Locate every leukocyte (white blood cell).
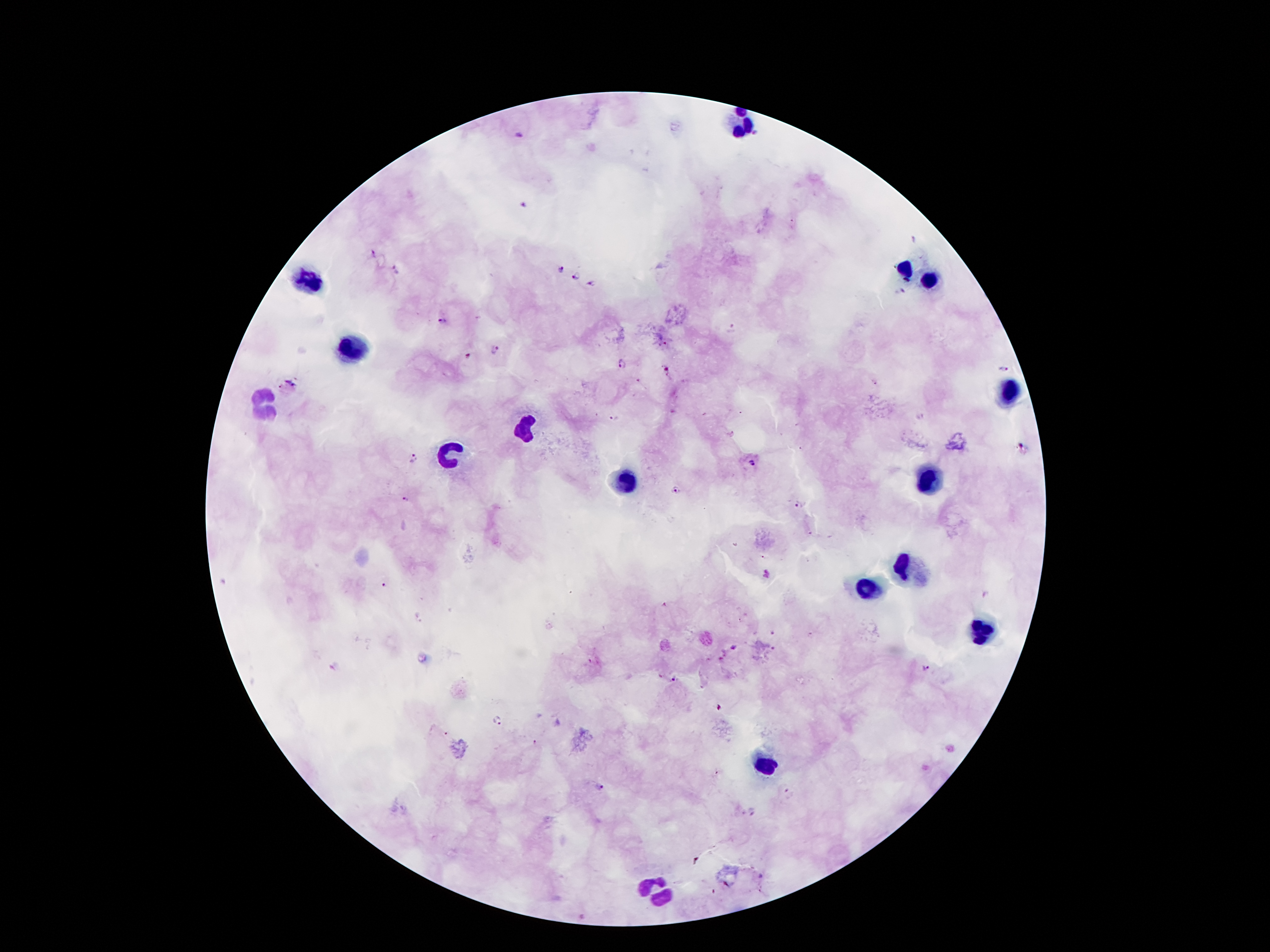

Approximate centers as {x, y} in pixels.
Leukocytes: {745, 123}, {907, 272}, {311, 281}, {929, 281}, {352, 353}, {1010, 390}, {268, 400}, {524, 428}, {444, 451}, {934, 480}, {625, 483}, {899, 569}, {865, 587}, {981, 632}, {766, 763}, {655, 890}.

{
  "magnification": "100x",
  "image_size": "1270×952 pixels",
  "preparation": "thick blood smear",
  "stain": "Giemsa",
  "capture": "smartphone through the microscope eyepiece",
  "patient_malaria_status": "positive for Plasmodium falciparum",
  "malaria_parasite_locations": "approximate centers as {x, y} in pixels: {756, 134}, {519, 135}, {371, 253}, {561, 268}, {396, 270}, {576, 276}, {592, 285}, {900, 293}, {441, 322}, {731, 328}, {496, 349}, {469, 356}, {623, 363}, {1001, 368}, {872, 383}, {614, 419}, {412, 459}, {753, 463}, {674, 490}, {408, 500}, {799, 505}, {767, 574}, {383, 585}, {772, 635}, {733, 649}, {334, 667}, {926, 668}, {674, 680}, {499, 721}, {537, 742}, {599, 788}, {790, 793}, {752, 811}",
  "field_of_view": "single"
}